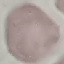

Summary:
  - Result: no malaria parasites seen
  - Image type: automatically extracted cell patch, resized to 64 × 64 pixels
  - Stain: Giemsa
  - Preparation: thin smear
  - Capture: smartphone camera at the microscope eyepiece